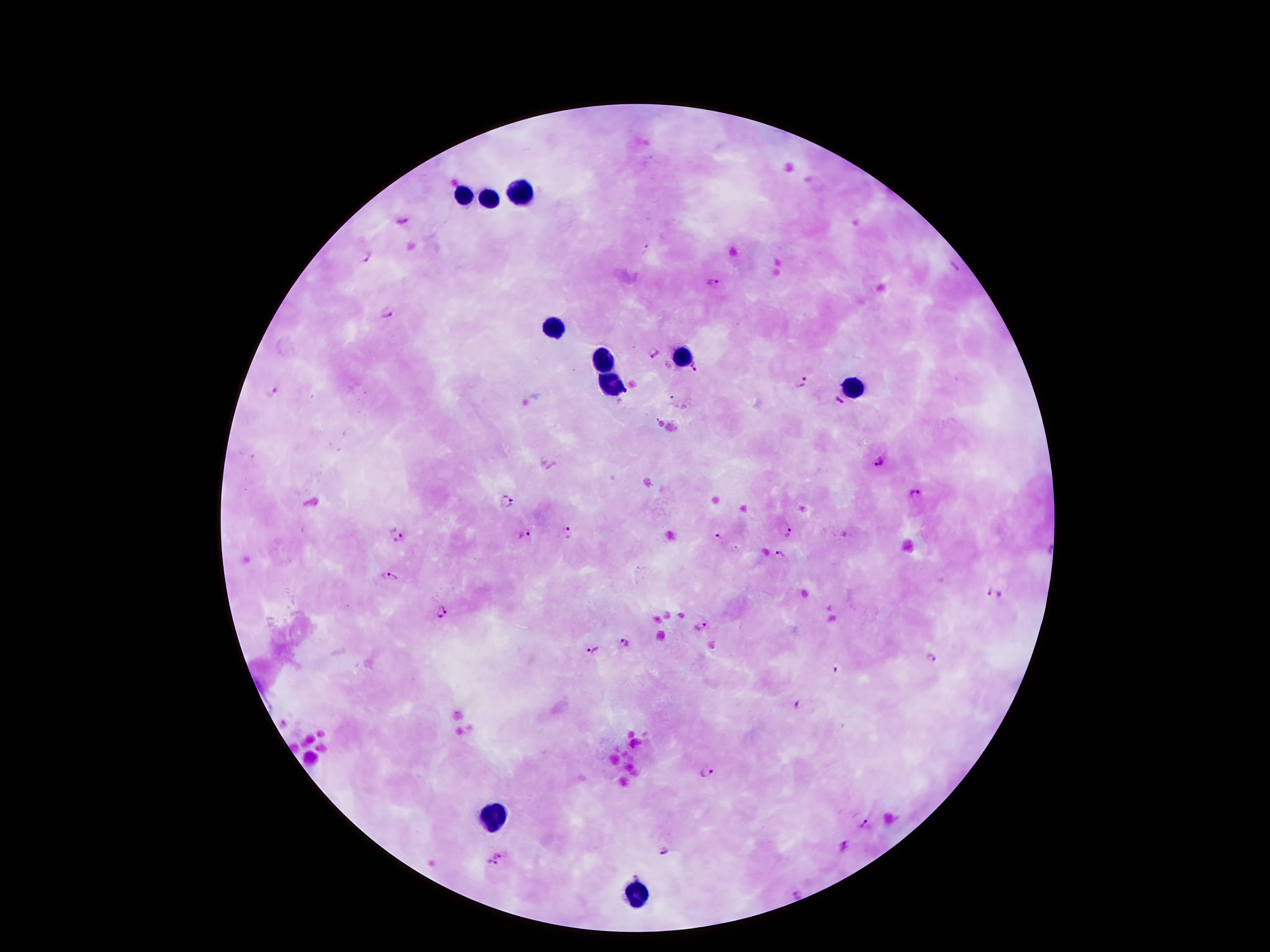

Approximate centers as (x, y) in pixels. Plasmodium parasite locations: (403, 222), (366, 256), (713, 284), (387, 313), (653, 353), (694, 369), (803, 382), (271, 392), (838, 403), (877, 463), (917, 495), (507, 501), (787, 533), (570, 534), (523, 535), (398, 536), (717, 538), (780, 553), (388, 576), (994, 596), (440, 611), (700, 626), (625, 643), (592, 650), (931, 658), (836, 670), (795, 705), (707, 771), (868, 823), (842, 846), (498, 849), (667, 850), (490, 865), (637, 872), (795, 896). Leukocyte locations: (525, 191), (465, 193), (488, 199), (553, 326), (685, 356), (607, 363), (611, 383), (855, 385), (492, 817), (633, 891). Giemsa stain. Smartphone photograph taken through the microscope eyepiece. Image is 1270×952 pixels. Thick blood smear. Patient malaria status: infected with Plasmodium falciparum. One field from this slide. 100x magnification.